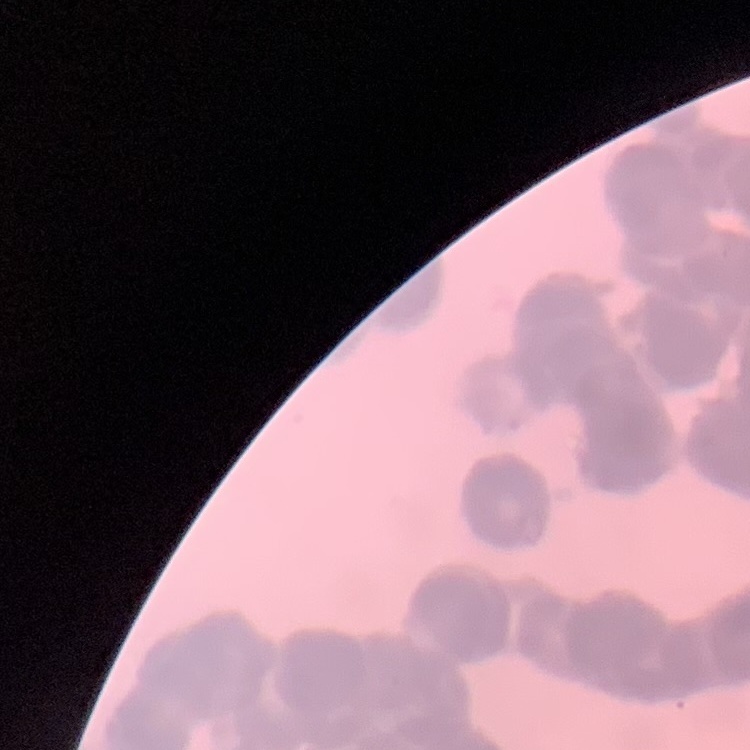
Summary:
  - Erythrocyte morphology: rouleaux formation
  - Stain: Field's or Giemsa
  - Preparation: thin blood smear
  - Image type: square crop of a larger photomicrograph